Report the malaria status of this cell.
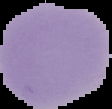
Uninfected.

image type = segmented cell region on a black background
image size = 112×109 pixels
preparation = thin blood smear